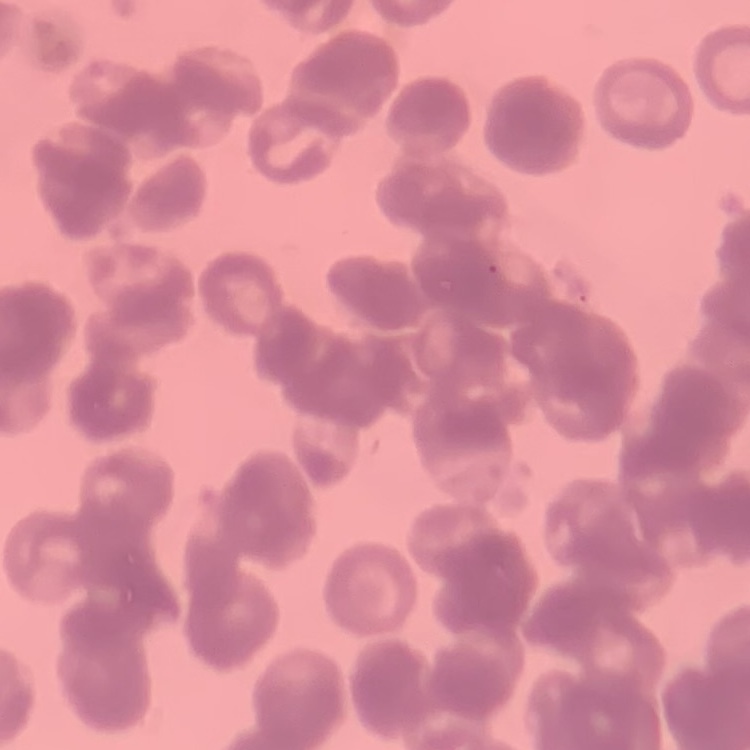 The erythrocytes show rouleaux formation. Thin peripheral smear. Field's or Giemsa stain. One tile cut from a larger photomicrograph.